Name the blood parasite species.
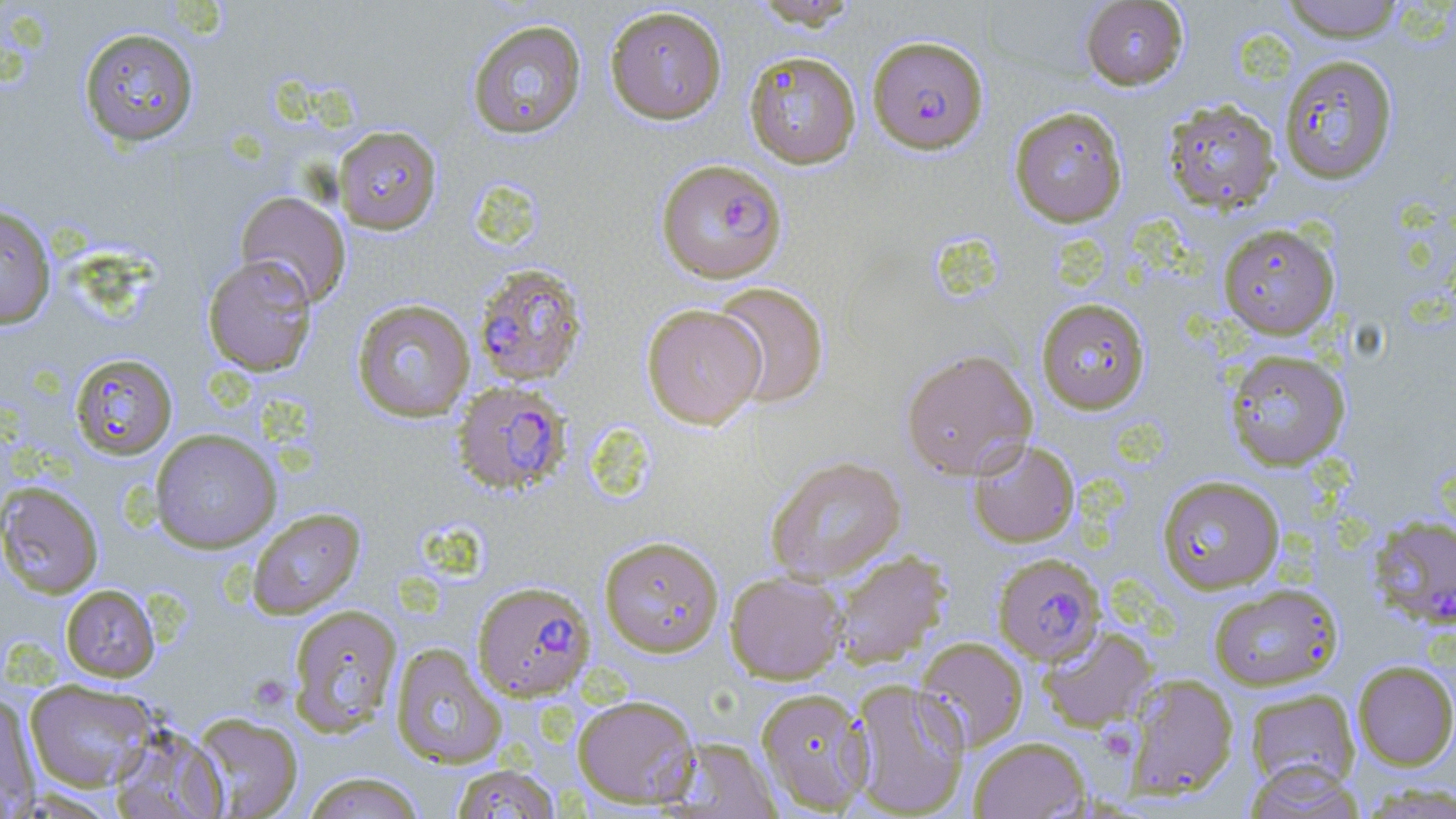
Plasmodium falciparum.

uninfected red blood cell locations (subset) = approximate bounding boxes as (x1,y1)-(x2,y2) corner pairs in pixels: (748,0)-(862,29), (1278,0)-(1408,41), (1080,1)-(1188,90), (604,6)-(727,124), (466,19)-(587,139), (77,26)-(200,148), (744,50)-(861,169), (1278,54)-(1399,185), (1161,98)-(1281,214), (1008,106)-(1128,227), (333,125)-(442,234), (235,191)-(351,307), (0,204)-(56,330), (1218,223)-(1340,339), (202,255)-(318,376), (711,281)-(829,408), (351,298)-(476,422), (1036,298)-(1151,414), (640,304)-(766,429), (900,348)-(1038,480), (1223,348)-(1350,471), (69,352)-(178,460), (149,428)-(282,553), (967,438)-(1080,547), (765,455)-(906,584), (1157,474)-(1285,593), (0,481)-(104,598), (246,507)-(366,618), (599,535)-(725,657), (829,549)-(951,669), (724,571)-(848,684), (1208,583)-(1343,691), (60,585)-(160,682), (287,603)-(403,736), (1038,625)-(1157,732), (914,636)-(1028,751), (390,643)-(507,769), (1352,660)-(1456,770), (1124,673)-(1239,799), (847,678)-(970,818), (24,679)-(159,791), (756,688)-(872,813), (1244,688)-(1360,791), (0,692)-(40,816), (572,694)-(700,809), (189,712)-(304,819), (108,723)-(228,819), (663,736)-(782,818), (969,736)-(1090,818), (1242,761)-(1364,819), (450,763)-(562,819), (300,771)-(426,818)
Plasmodium falciparum-infected red blood cell locations (subset) = approximate bounding boxes as (x1,y1)-(x2,y2) corner pairs in pixels: (867,35)-(988,154), (660,159)-(792,284), (472,263)-(588,387), (1368,514)-(1456,629), (992,552)-(1105,664), (472,580)-(596,700)
field of view = single
modality = light microscopy
stain = May-Grünwald-Giemsa
platelet locations = approximate bounding boxes as (x1,y1)-(x2,y2) corner pairs in pixels: (251,671)-(290,714), (1101,730)-(1130,753)
image size = 1456×819 pixels
preparation = thin blood smear
magnification = 1000x